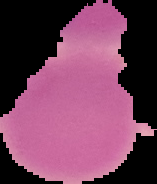

image type = segmented cell region on a black background
preparation = thin blood film
image size = 157×184 pixels
malaria status = uninfected